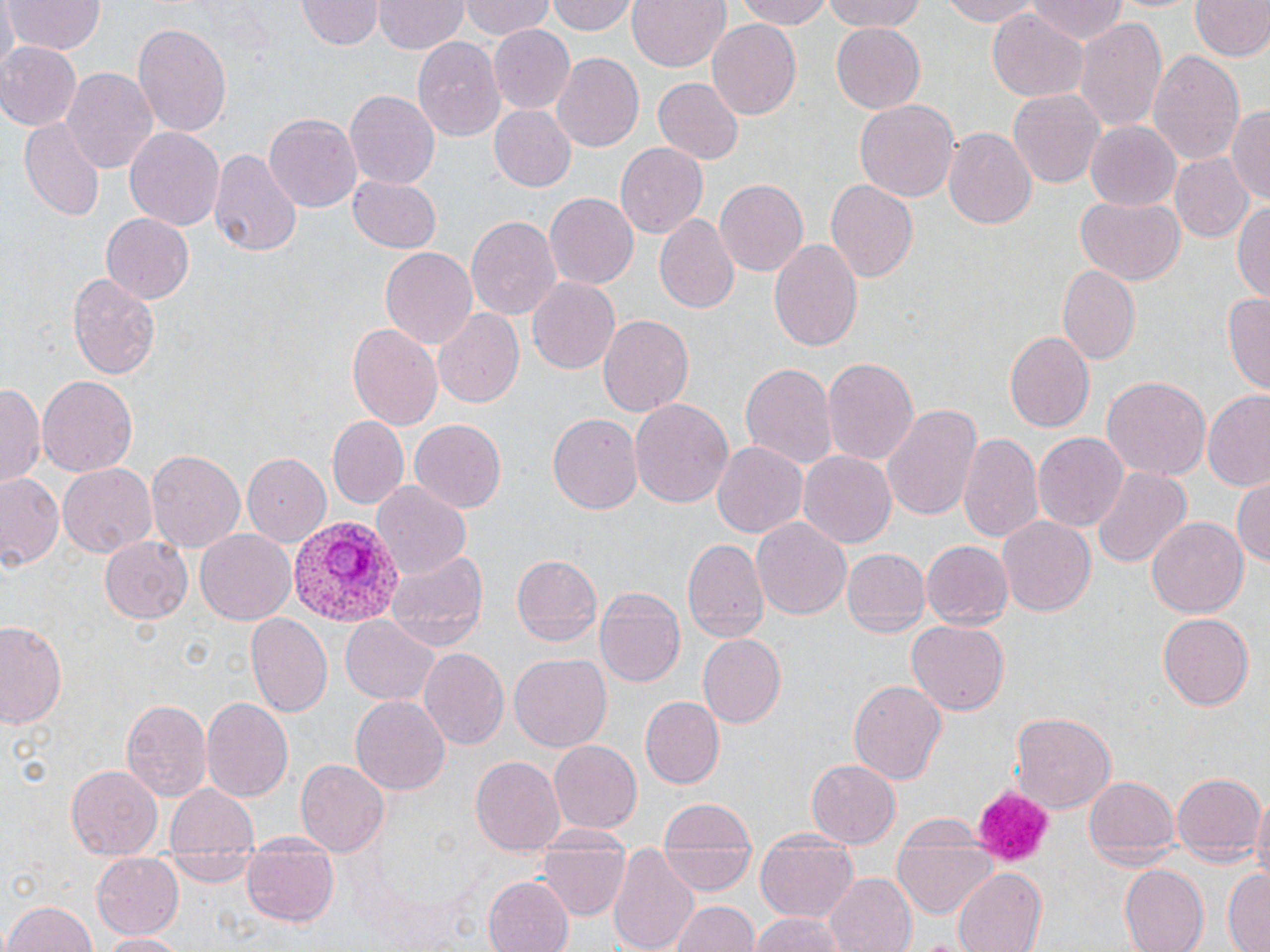

Approximate bounding boxes as [x1, y1, x2, y2] in pixels. Plasmodium vivax-infected red blood cell locations: [289, 513, 405, 628]. Platelet locations: [970, 789, 1057, 865]. Uninfected red blood cell locations: [5, 0, 105, 54], [462, 0, 556, 40], [547, 0, 638, 37], [626, 0, 729, 74], [738, 0, 835, 28], [824, 0, 927, 34], [933, 0, 1052, 27], [1189, 0, 1268, 60], [375, 1, 468, 54], [1024, 1, 1131, 45], [298, 2, 382, 51], [989, 8, 1088, 99], [1073, 15, 1169, 137], [706, 20, 801, 121], [133, 22, 231, 137], [487, 25, 576, 114], [832, 25, 925, 113], [413, 36, 504, 143], [0, 42, 80, 133], [1149, 49, 1245, 168], [551, 54, 644, 153], [62, 67, 157, 177], [652, 77, 742, 165], [1008, 87, 1105, 191], [344, 89, 438, 190], [855, 99, 959, 201], [488, 104, 576, 193], [1228, 105, 1269, 207], [264, 112, 361, 212], [20, 119, 108, 218], [1085, 122, 1181, 212], [123, 125, 225, 231], [943, 127, 1037, 229], [614, 140, 707, 236], [209, 145, 300, 259], [1171, 155, 1254, 244], [347, 172, 440, 252], [715, 178, 811, 276], [824, 178, 918, 283], [545, 192, 638, 288], [1076, 195, 1184, 284], [1234, 198, 1270, 303], [102, 213, 194, 302], [654, 213, 741, 314], [466, 214, 562, 322], [769, 237, 863, 356], [380, 246, 476, 349], [1059, 266, 1139, 364], [66, 272, 162, 379], [527, 277, 621, 375], [1223, 293, 1270, 391], [433, 308, 524, 408], [596, 311, 693, 416], [348, 323, 441, 432], [1001, 330, 1094, 433], [821, 357, 916, 467], [739, 361, 835, 470], [37, 374, 138, 479], [1102, 374, 1208, 479], [0, 384, 41, 487], [1201, 392, 1270, 488], [631, 396, 732, 509], [880, 404, 980, 522], [548, 412, 642, 515], [327, 418, 410, 505], [408, 419, 505, 512], [958, 430, 1042, 542], [1033, 432, 1128, 530], [710, 441, 807, 539], [147, 450, 245, 552], [799, 451, 896, 547], [241, 453, 330, 547], [58, 463, 156, 557], [1088, 467, 1190, 570], [0, 473, 64, 573], [1231, 473, 1269, 569], [372, 479, 471, 580], [996, 515, 1097, 619], [1147, 515, 1247, 621], [751, 516, 851, 622], [196, 529, 295, 622], [99, 534, 192, 625], [681, 538, 766, 641], [921, 541, 1012, 629], [843, 547, 929, 638], [387, 549, 486, 650], [512, 553, 604, 646], [596, 587, 686, 688], [246, 612, 333, 718], [1157, 612, 1255, 710], [341, 616, 437, 706], [906, 618, 1010, 715], [0, 619, 68, 729], [696, 635, 784, 726], [419, 646, 508, 750], [509, 653, 612, 751], [847, 678, 946, 785], [351, 694, 449, 795], [200, 696, 291, 802], [640, 697, 723, 788], [120, 698, 211, 801], [1012, 711, 1116, 810], [548, 738, 643, 831], [470, 755, 565, 855], [296, 758, 388, 857], [805, 758, 901, 847], [66, 763, 164, 858], [1171, 772, 1263, 865], [1085, 775, 1179, 867], [167, 782, 260, 855], [1249, 791, 1270, 887], [656, 799, 755, 851], [889, 822, 998, 921], [755, 835, 858, 922], [240, 841, 339, 927], [536, 847, 627, 918], [607, 847, 698, 952], [658, 848, 756, 893], [90, 855, 183, 938], [1119, 863, 1209, 951], [1221, 867, 1270, 951], [953, 868, 1049, 952], [824, 873, 916, 952], [482, 876, 573, 952], [3, 898, 97, 952], [668, 899, 759, 952], [747, 912, 856, 952], [100, 932, 185, 952]. Slide-level diagnosis: Plasmodium vivax. Optical microscopy. 1000x magnification. Image is 1270×952 pixels. One field of a larger specimen. Thin blood smear. May-Grünwald-Giemsa-stained preparation.